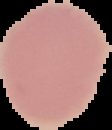
Image is 112×130 pixels. Malaria status: uninfected. From a thin blood film. Cell region segmented out of the field of view; the surrounding area is masked to black.